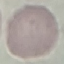

Summary:
  - Result: no malaria parasites seen
  - Preparation: thin blood smear
  - Capture: smartphone camera at the microscope eyepiece
  - Image type: automatically extracted cell patch, resized to 64 × 64 pixels
  - Stain: Giemsa